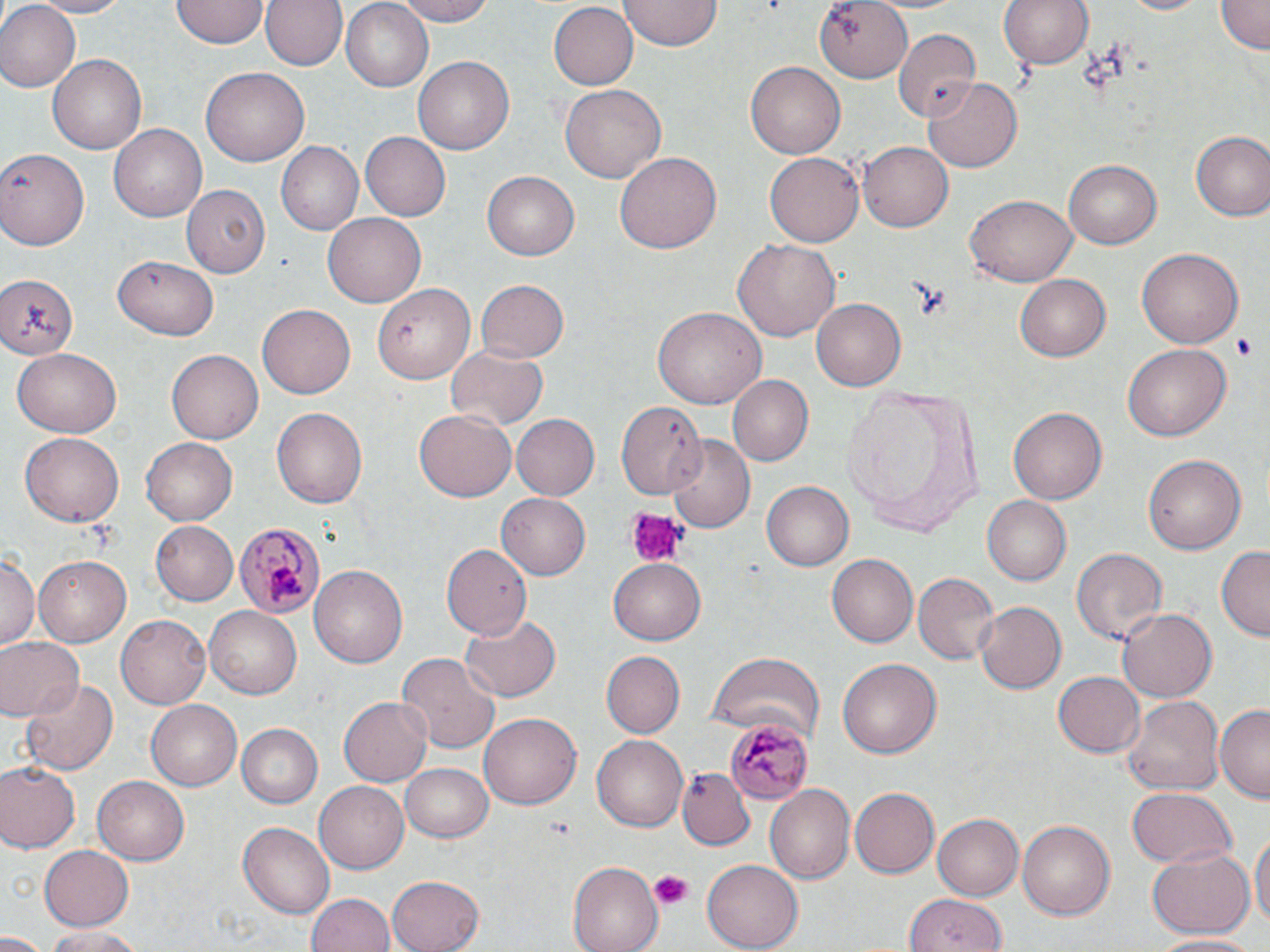 Approximate bounding boxes as [x1, y1, x2, y2] in pixels. Uninfected red blood cell locations: [23, 0, 135, 16], [172, 0, 266, 48], [263, 0, 347, 72], [341, 0, 433, 88], [388, 0, 497, 25], [809, 0, 914, 81], [998, 0, 1094, 74], [1115, 0, 1215, 17], [1217, 0, 1268, 53], [0, 1, 78, 91], [549, 1, 637, 87], [620, 1, 720, 52], [892, 29, 982, 118], [49, 54, 146, 155], [415, 57, 513, 156], [746, 62, 845, 159], [201, 67, 309, 166], [925, 78, 1023, 173], [559, 84, 666, 185], [109, 122, 208, 221], [1190, 131, 1270, 220], [360, 132, 449, 219], [860, 139, 955, 232], [277, 142, 363, 234], [0, 146, 90, 250], [614, 152, 722, 255], [765, 153, 863, 246], [1062, 158, 1163, 248], [481, 170, 581, 263], [184, 184, 271, 278], [965, 194, 1077, 287], [323, 214, 424, 307], [733, 239, 842, 342], [1136, 246, 1242, 349], [115, 253, 216, 341], [0, 274, 81, 360], [1015, 274, 1112, 362], [474, 279, 568, 365], [375, 280, 478, 384], [811, 297, 905, 390], [258, 305, 355, 399], [652, 305, 765, 411], [1122, 343, 1230, 444], [167, 347, 262, 441], [445, 347, 547, 431], [13, 349, 120, 437], [727, 375, 813, 467], [841, 383, 986, 538], [614, 401, 706, 501], [1008, 406, 1105, 505], [271, 407, 368, 509], [414, 409, 515, 502], [511, 414, 599, 500], [19, 431, 123, 527], [141, 436, 239, 526], [664, 436, 755, 532], [1142, 453, 1247, 554], [761, 481, 853, 571], [497, 492, 590, 579], [982, 497, 1071, 587], [151, 520, 238, 605], [440, 542, 531, 641], [1216, 544, 1270, 641], [1071, 548, 1166, 648], [0, 554, 40, 652], [826, 554, 919, 647], [35, 555, 133, 646], [610, 557, 707, 642], [309, 565, 407, 669], [914, 571, 999, 663], [975, 600, 1067, 695], [205, 608, 302, 698], [1116, 609, 1216, 703], [460, 614, 560, 704], [116, 615, 211, 710], [0, 637, 80, 721], [599, 651, 684, 737], [707, 651, 823, 739], [395, 652, 502, 752], [836, 658, 943, 761], [1053, 671, 1145, 757], [20, 678, 117, 776], [338, 696, 434, 787], [1119, 696, 1223, 796], [145, 701, 242, 791], [1214, 702, 1270, 802], [479, 710, 581, 805], [235, 724, 323, 808], [592, 735, 688, 832], [0, 761, 78, 852], [400, 763, 493, 843], [679, 768, 754, 849], [92, 774, 191, 865], [315, 782, 408, 875], [767, 784, 856, 882], [849, 786, 940, 878], [1125, 788, 1237, 870], [932, 812, 1023, 901], [1017, 820, 1115, 918], [239, 822, 333, 916], [1251, 828, 1269, 939], [39, 843, 134, 929], [1146, 845, 1255, 940], [703, 858, 802, 949], [567, 862, 662, 952], [386, 874, 483, 952], [307, 891, 399, 952], [906, 895, 1008, 952], [39, 925, 148, 950], [0, 933, 51, 952], [1150, 933, 1265, 950]. Plasmodium malariae-infected red blood cell locations: [233, 521, 323, 619], [725, 716, 812, 802]. Platelet locations: [626, 509, 685, 565], [650, 870, 694, 908]. Slide-level diagnosis: Plasmodium malariae. One field of a larger specimen. May-Grünwald-Giemsa stain. Optical microscopy. Thin blood film. 1000x magnification. Image is 1270×952 pixels.